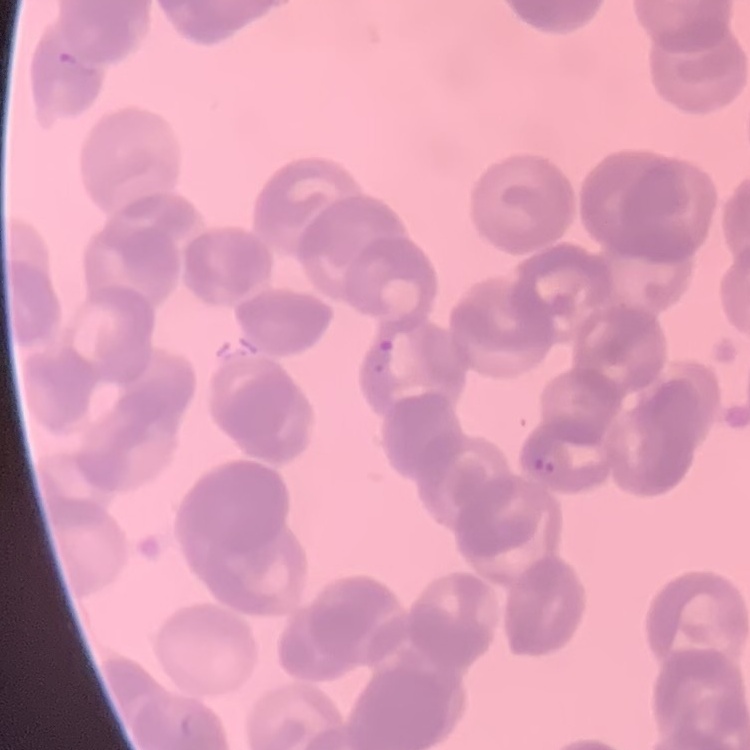

The erythrocytes show rouleaux formation. Thin blood film. One tile cut from a larger photomicrograph. Field's or Giemsa stain.